Assess for malaria.
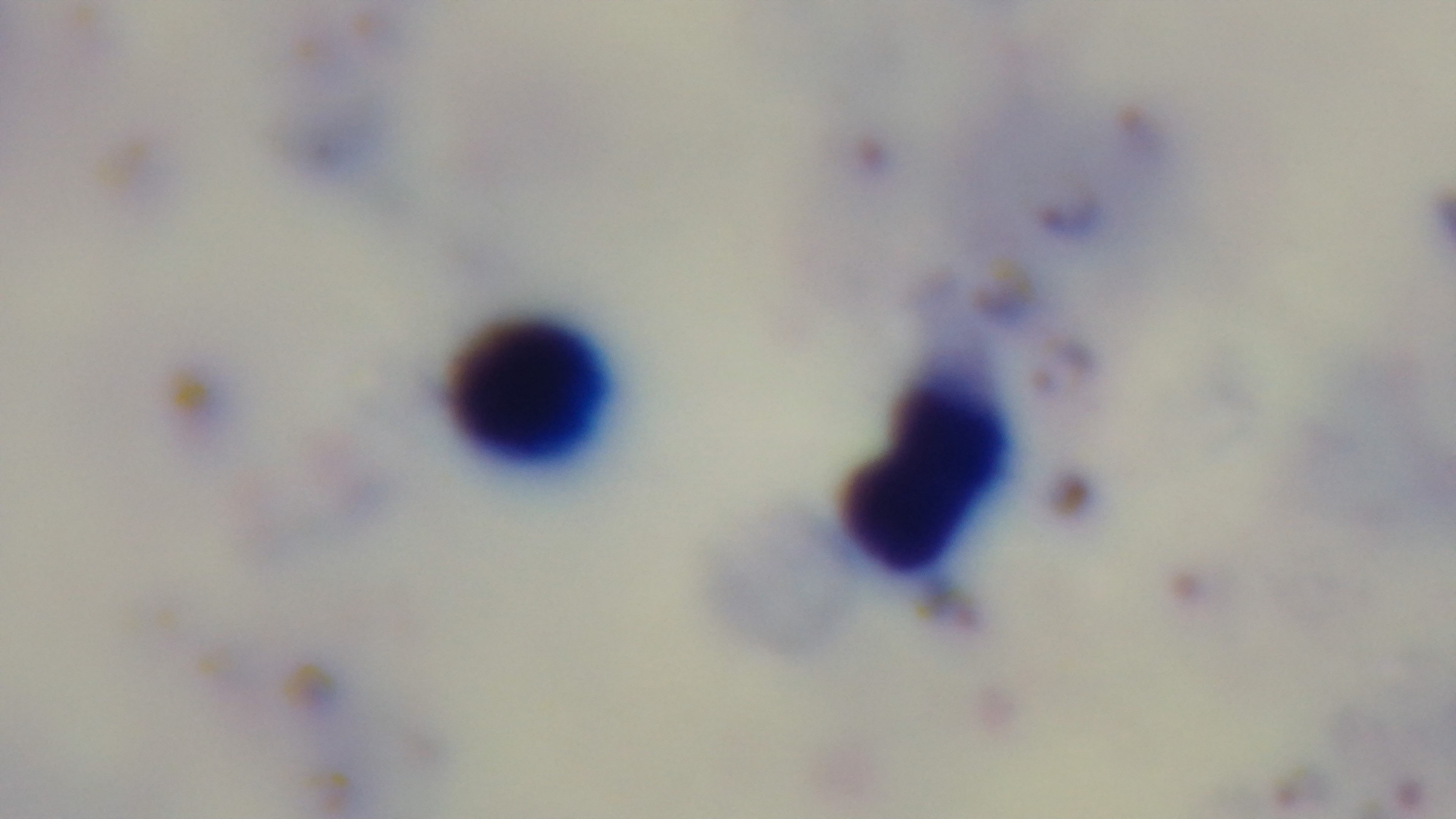

Infected.

Summary:
  - Field of view: one from the slide
  - Objective: 100x oil immersion
  - Modality: light microscopy
  - Preparation: thick blood film
  - Stain: Giemsa
  - Capture: mounted 4K digital camera